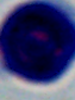
Summary:
  - Modality: photomicrograph
  - Identification: white blood cell
  - Magnification: 1000x